Give the extent of all Plasmodium vivax-infected red blood cells.
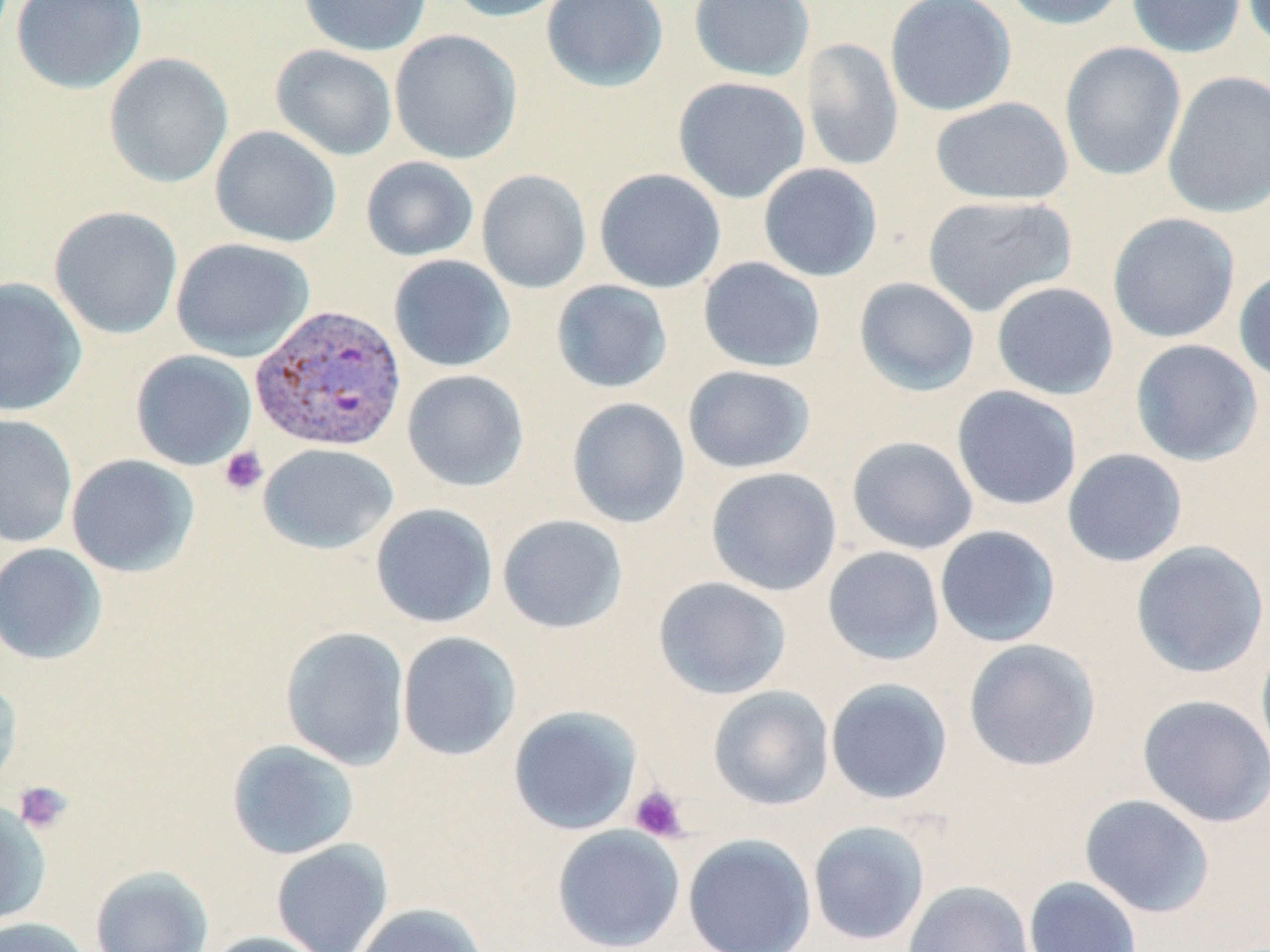
Approximate bounding boxes as (x1,y1)-(x2,y2) corner pairs in pixels.
Plasmodium vivax-infected red blood cells: (249,304)-(407,454).

slide-level diagnosis = Plasmodium vivax
modality = light microscopy
image size = 1270×952 pixels
platelet locations = approximate bounding boxes as (x1,y1)-(x2,y2) corner pairs in pixels: (219,446)-(268,496), (13,780)-(74,834), (629,784)-(689,842)
uninfected red blood cell locations = approximate bounding boxes as (x1,y1)-(x2,y2) corner pairs in pixels: (10,0)-(148,94), (298,0)-(432,57), (445,0)-(574,22), (541,0)-(668,92), (688,0)-(815,82), (885,0)-(1016,117), (999,0)-(1131,30), (1126,0)-(1246,59), (1240,0)-(1270,53), (389,29)-(523,165), (800,37)-(904,172), (1059,41)-(1187,182), (270,44)-(398,162), (103,53)-(233,189), (1162,71)-(1270,218), (672,76)-(810,204), (929,97)-(1074,205), (209,125)-(342,248), (360,156)-(479,262), (758,163)-(883,282), (594,168)-(726,293), (476,169)-(592,294), (921,194)-(1078,317), (49,206)-(183,340), (1107,212)-(1240,344), (170,237)-(315,361), (388,254)-(515,372), (698,257)-(826,373), (1234,266)-(1270,385), (0,277)-(87,417), (853,277)-(980,397), (551,279)-(673,394), (991,282)-(1119,400), (1129,339)-(1263,466), (130,349)-(256,470), (683,365)-(816,474), (402,369)-(529,492), (951,385)-(1082,511), (566,397)-(690,528), (0,414)-(78,548), (846,436)-(978,555), (258,443)-(399,554), (1061,448)-(1188,568), (65,454)-(199,577), (705,466)-(842,596), (369,503)-(498,628), (497,514)-(628,634), (934,525)-(1061,647), (1130,540)-(1269,678), (0,543)-(107,665), (822,546)-(945,666), (653,576)-(792,699), (279,626)-(410,770), (396,631)-(521,761), (1255,637)-(1270,769), (962,638)-(1101,772), (0,677)-(22,797), (825,678)-(953,805), (707,685)-(835,810), (1136,694)-(1270,827), (509,705)-(642,835), (226,739)-(360,860), (1079,793)-(1215,918), (0,800)-(52,928), (807,820)-(930,947), (551,825)-(686,951), (682,833)-(817,952), (271,839)-(393,952), (89,864)-(215,952), (1023,876)-(1143,952), (903,879)-(1034,952), (351,902)-(489,952), (0,917)-(94,952), (201,931)-(333,952)
field of view = single
stain = May-Grünwald-Giemsa
magnification = 1000x
preparation = thin blood smear